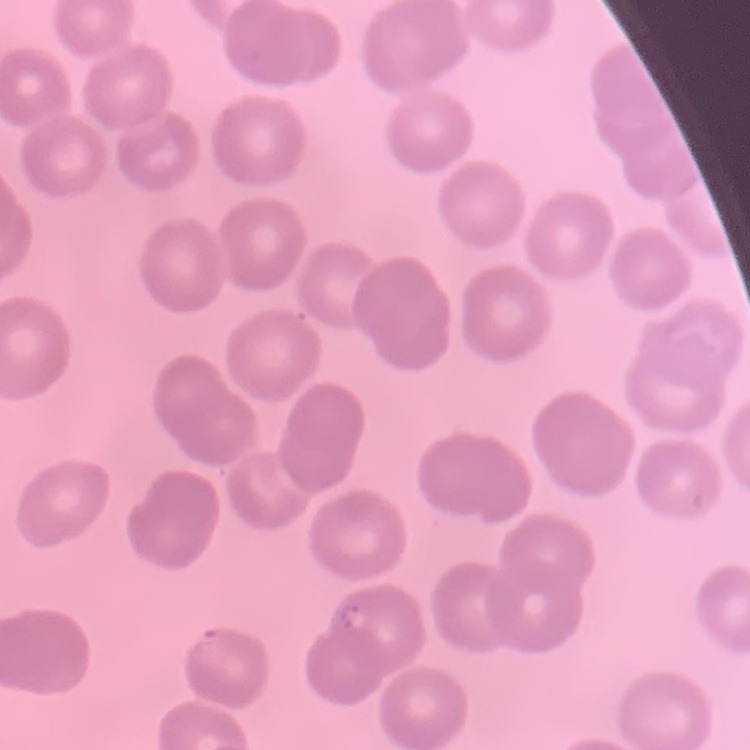

erythrocyte_morphology: no rouleaux formation
image_type: one tile cut from a larger photomicrograph
preparation: thin peripheral smear
stain: Field's or Giemsa